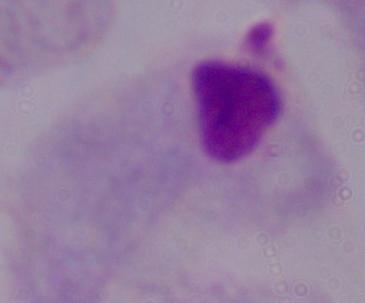

identification = trichomonad
magnification = 1000x
modality = photomicrograph